Identify the preparation type.
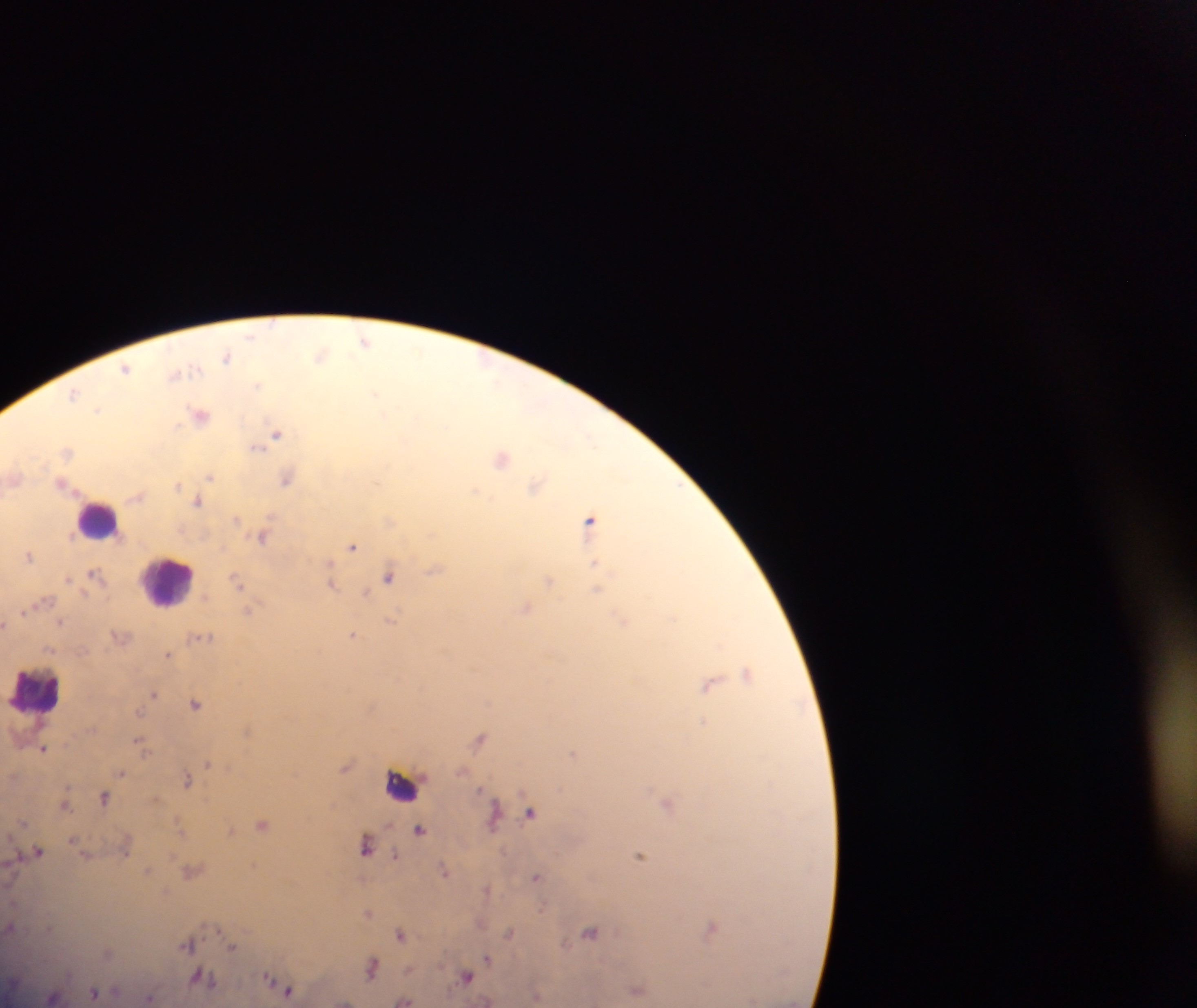

Thick blood smear.

capture = mobile-phone photograph through a microscope
country = Ghana
leukocyte locations = approximate centers as [x, y] in pixels: [99, 519], [169, 579], [37, 689]
malaria parasite locations = approximate centers as [x, y] in pixels: [252, 335], [364, 341], [321, 354], [227, 357], [126, 368], [179, 372], [257, 384], [374, 392], [73, 394], [98, 408], [200, 414], [276, 433], [256, 446], [67, 451], [503, 458], [210, 476], [286, 477], [62, 483], [177, 485], [535, 485], [476, 491], [198, 501], [237, 519], [589, 519], [390, 520], [263, 536], [351, 546], [28, 554], [596, 565], [435, 569], [95, 574], [389, 576], [236, 580], [549, 580], [330, 583], [597, 589], [366, 593], [45, 600], [525, 607], [247, 611], [673, 617], [621, 619], [391, 620], [61, 621], [352, 634], [201, 637], [169, 654], [748, 672], [709, 684], [154, 692], [195, 703], [702, 721], [246, 731], [480, 737], [140, 743], [43, 747], [573, 753], [208, 763], [345, 766], [122, 772], [186, 779], [103, 798], [667, 803], [64, 804], [530, 811], [494, 816], [262, 824], [420, 829], [230, 831], [125, 844], [365, 846], [37, 852], [639, 855], [396, 856], [148, 870], [444, 870], [191, 871], [537, 876], [486, 888], [367, 912], [10, 927], [710, 928], [508, 932], [590, 932], [400, 934], [188, 943], [232, 946], [487, 957], [372, 967], [466, 976], [204, 977], [270, 981], [286, 989], [637, 990], [95, 992], [149, 998], [404, 1000]
field of view = single
object labeled both malaria parasite and leukocyte by the source = approximate centers as [x, y] in pixels: [401, 784]
image size = 1197×1008 pixels